Locate and identify every blood parasite.
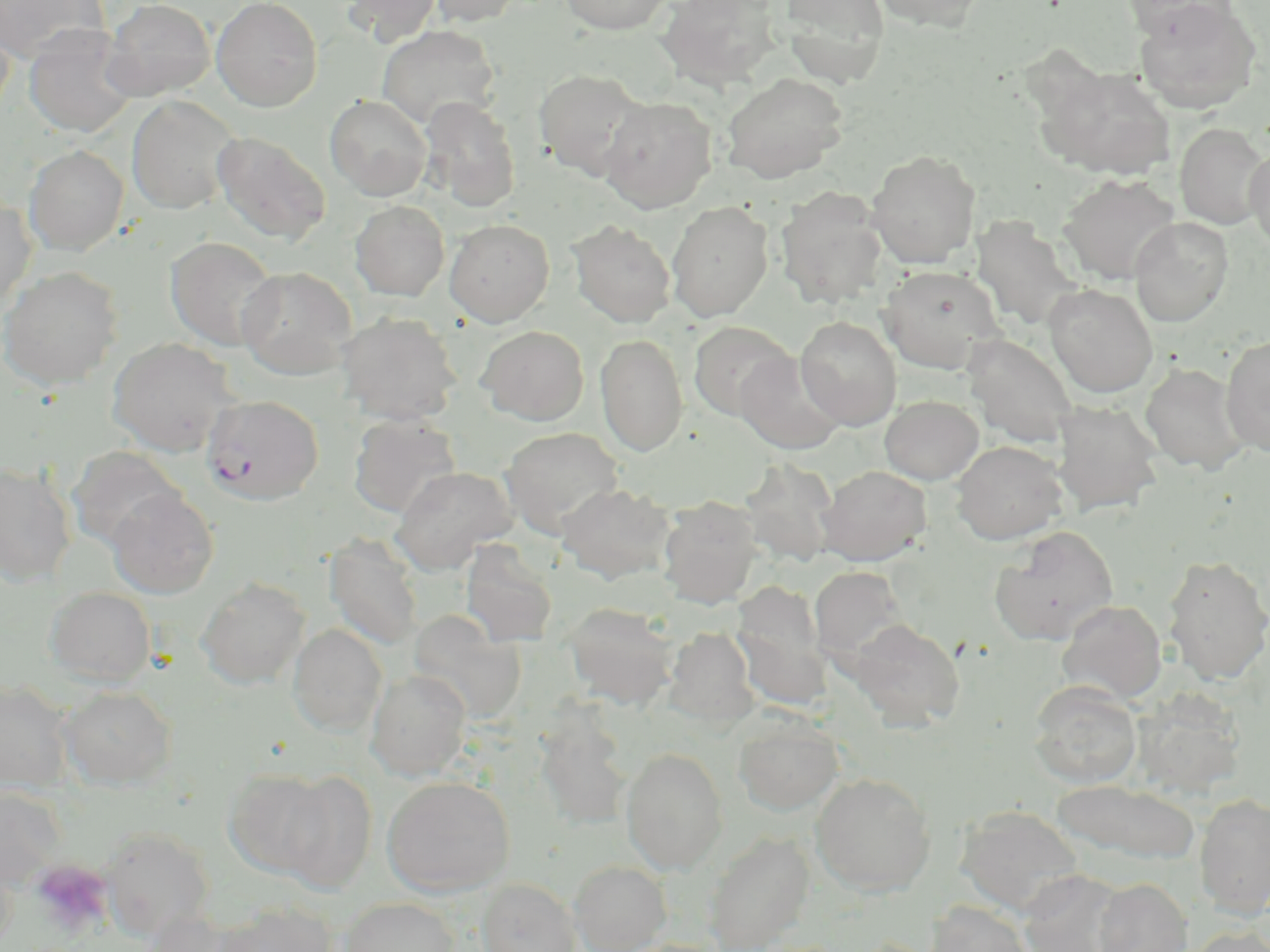

Approximate bounding boxes as [x1, y1, x2, y2] in pixels.
Plasmodium falciparum-infected red blood cells: [202, 393, 324, 505].
No Plasmodium ovale, Plasmodium malariae, Plasmodium vivax, Babesia divergens, or Trypanosoma brucei observed.

slide-level diagnosis = Plasmodium falciparum
magnification = 1000x
field of view = one of a larger specimen
uninfected red blood cell locations = approximate bounding boxes as [x1, y1, x2, y2] in pixels: [0, 0, 109, 65], [101, 0, 215, 101], [211, 0, 323, 112], [341, 0, 442, 46], [425, 0, 525, 27], [558, 0, 673, 35], [779, 0, 891, 86], [872, 0, 986, 33], [1120, 0, 1240, 42], [656, 1, 784, 91], [113, 2, 221, 212], [1134, 3, 1262, 115], [0, 16, 14, 123], [23, 25, 139, 139], [377, 25, 501, 129], [1038, 64, 1177, 180], [532, 68, 651, 180], [720, 72, 849, 183], [325, 94, 431, 201], [126, 96, 241, 215], [419, 96, 521, 211], [599, 96, 718, 213], [1176, 123, 1269, 230], [212, 131, 331, 245], [23, 145, 129, 255], [1245, 146, 1270, 252], [866, 149, 981, 269], [1058, 173, 1181, 285], [775, 187, 888, 310], [0, 195, 37, 313], [350, 200, 450, 301], [666, 201, 774, 322], [970, 216, 1087, 333], [1128, 217, 1234, 327], [444, 219, 555, 327], [567, 220, 676, 327], [164, 236, 280, 351], [878, 265, 1006, 374], [0, 266, 123, 390], [236, 266, 356, 379], [1044, 283, 1158, 398], [336, 311, 462, 426], [795, 316, 901, 431], [689, 321, 795, 421], [478, 325, 589, 425], [596, 333, 688, 457], [961, 333, 1079, 448], [1220, 336, 1270, 457], [107, 337, 238, 456], [735, 351, 845, 455], [1139, 362, 1249, 475], [879, 395, 984, 485], [1050, 399, 1164, 516], [348, 415, 462, 518], [499, 426, 625, 538], [952, 440, 1067, 544], [66, 446, 185, 551], [739, 457, 840, 567], [0, 461, 78, 587], [817, 465, 931, 565], [391, 466, 518, 573], [557, 483, 676, 584], [106, 488, 219, 598], [657, 497, 762, 608], [990, 527, 1119, 645], [323, 534, 424, 651], [461, 541, 559, 647], [1163, 555, 1270, 685], [809, 566, 909, 663], [196, 577, 310, 690], [732, 582, 833, 708], [45, 587, 156, 687], [1056, 599, 1167, 704], [563, 601, 680, 709], [408, 610, 526, 723], [848, 619, 965, 730], [287, 624, 387, 735], [663, 626, 759, 727], [366, 669, 471, 781], [0, 680, 73, 792], [1029, 681, 1142, 788], [59, 686, 177, 789], [1130, 687, 1247, 799], [533, 703, 634, 830], [733, 717, 843, 815], [621, 748, 728, 874], [223, 768, 335, 879], [277, 770, 378, 893], [811, 772, 936, 896], [381, 776, 515, 897], [1051, 780, 1202, 867], [0, 784, 66, 890], [1195, 794, 1270, 918], [955, 804, 1086, 917], [98, 827, 216, 941], [704, 831, 815, 952], [0, 849, 18, 949], [569, 861, 671, 952], [1017, 869, 1129, 952], [475, 878, 581, 952], [1093, 878, 1192, 952], [340, 897, 460, 952], [926, 900, 1034, 952], [213, 901, 338, 952], [140, 910, 251, 952], [1184, 924, 1270, 952]
image size = 1270×952 pixels
modality = light microscopy
stain = May-Grünwald-Giemsa
preparation = thin blood film
platelet locations = approximate bounding boxes as [x1, y1, x2, y2] in pixels: [29, 860, 113, 937]